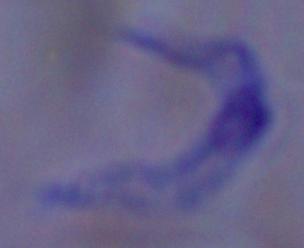
identification = trypanosome
modality = micrograph
magnification = 1000x